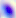
Captured at 400x magnification. Micrograph. Toxoplasma gondii is shown.